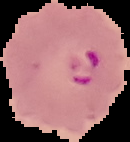

From a thin blood smear. Cell region segmented out of the field of view; the surrounding area is masked to black. Malaria status: parasitized. Image is 130×142 pixels.